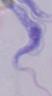

1000x magnification. A trypanosome is shown. Photomicrograph.